Name the parasite shown.
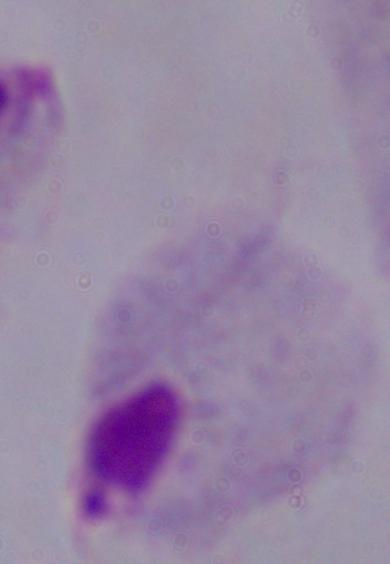

A trichomonad.

Summary:
  - Magnification: 1000x
  - Modality: photomicrograph